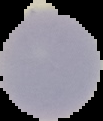
Summary:
  - Image type: segmented cell region on a black background
  - Result: negative for malaria parasites
  - Preparation: thin blood smear
  - Image size: 103×121 pixels